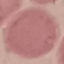
Malaria status: uninfected. Automatically extracted cell patch, resized to 64 × 64 pixels. Acquired by smartphone through the microscope eyepiece. Thin blood smear. Giemsa stain.